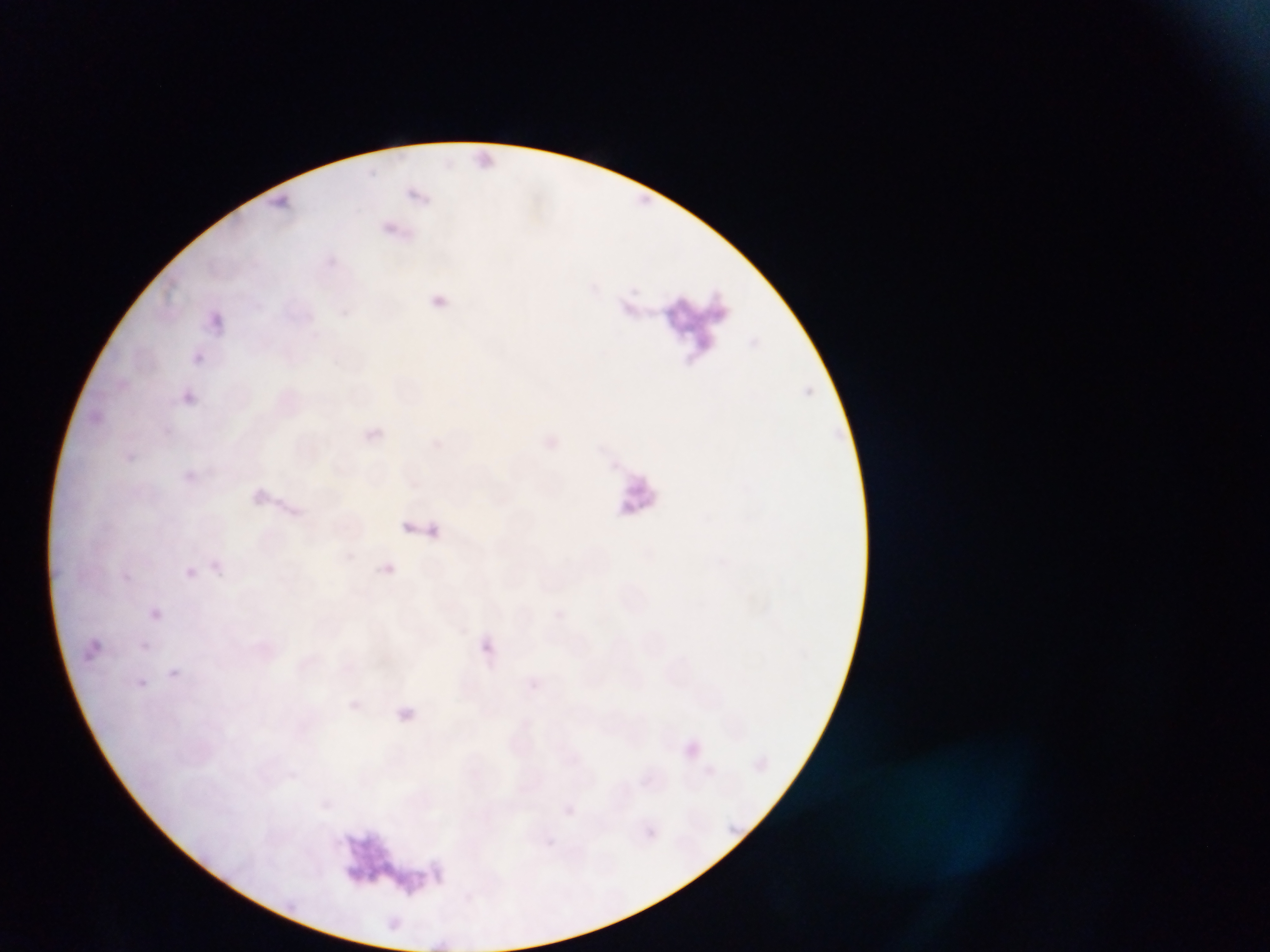

Approximate bounding boxes as [left, top, right, bottom] in pixels. Plasmodium parasite locations: [477, 150, 494, 166], [633, 185, 655, 210], [404, 187, 433, 211], [268, 192, 298, 211], [382, 219, 408, 238], [423, 288, 448, 305], [620, 301, 635, 315], [203, 310, 228, 327], [193, 352, 205, 363], [182, 387, 206, 413], [363, 423, 392, 452], [179, 467, 205, 486], [244, 485, 295, 516], [401, 511, 442, 531], [384, 563, 396, 573], [185, 567, 196, 578], [143, 600, 167, 622], [78, 636, 99, 661], [481, 639, 495, 657], [168, 669, 181, 679], [138, 678, 148, 688], [528, 679, 540, 690], [384, 699, 417, 729], [681, 735, 714, 761], [755, 749, 780, 773], [642, 772, 653, 783], [321, 798, 332, 808], [563, 804, 574, 815], [722, 813, 748, 839], [647, 828, 656, 837], [279, 891, 317, 922], [389, 915, 413, 936]. One field of view. Image is 1270×952 pixels. Photographed through a microscope with a mobile-phone camera. Thin blood film. Collected in Ghana.